Assess the morphology of the erythrocytes.
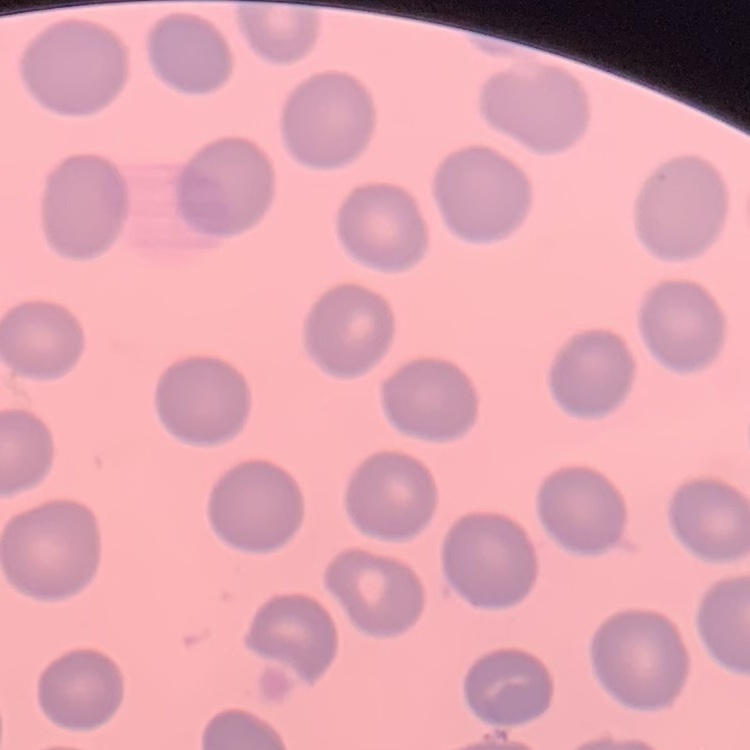
No rouleaux formation.

stain = Field's or Giemsa
preparation = thin blood film
image type = square crop of a larger photomicrograph